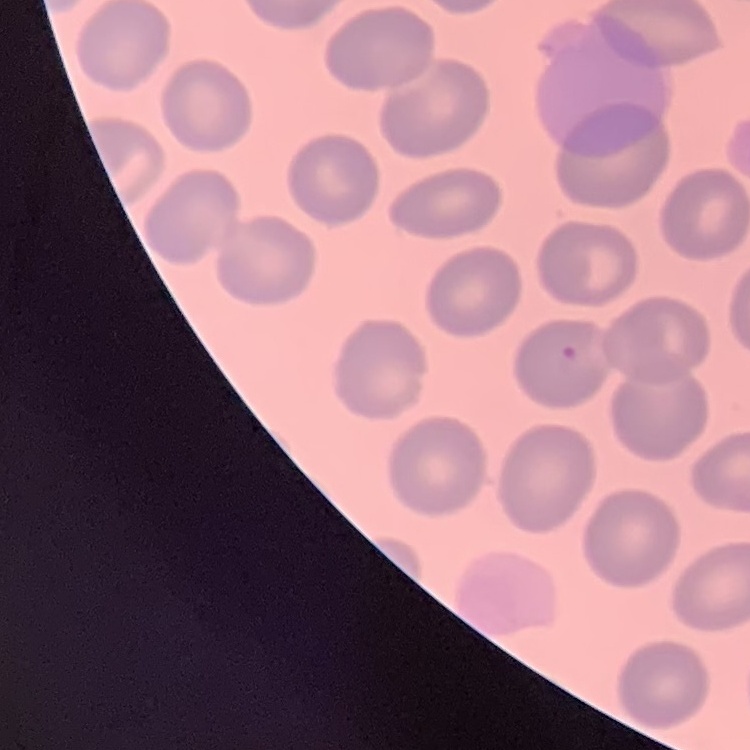

Summary:
  - Red blood cell morphology: no rouleaux formation
  - Preparation: thin peripheral smear
  - Image type: square crop of a larger photomicrograph
  - Stain: Field's or Giemsa